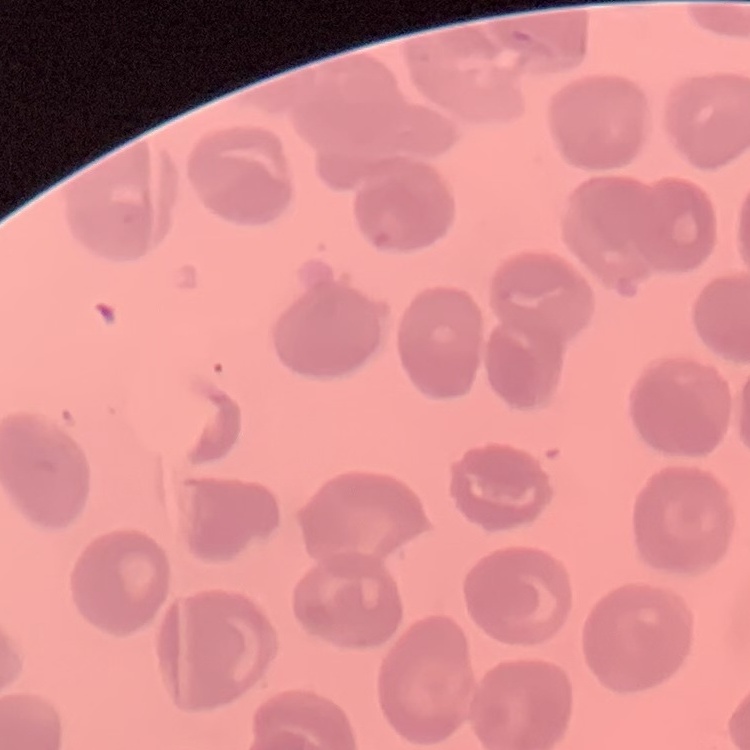

Summary:
  - Erythrocyte morphology: no rouleaux formation
  - Preparation: thin peripheral smear
  - Stain: Field's or Giemsa
  - Image type: square crop of a larger photomicrograph